Outline each blood parasite and name the species.
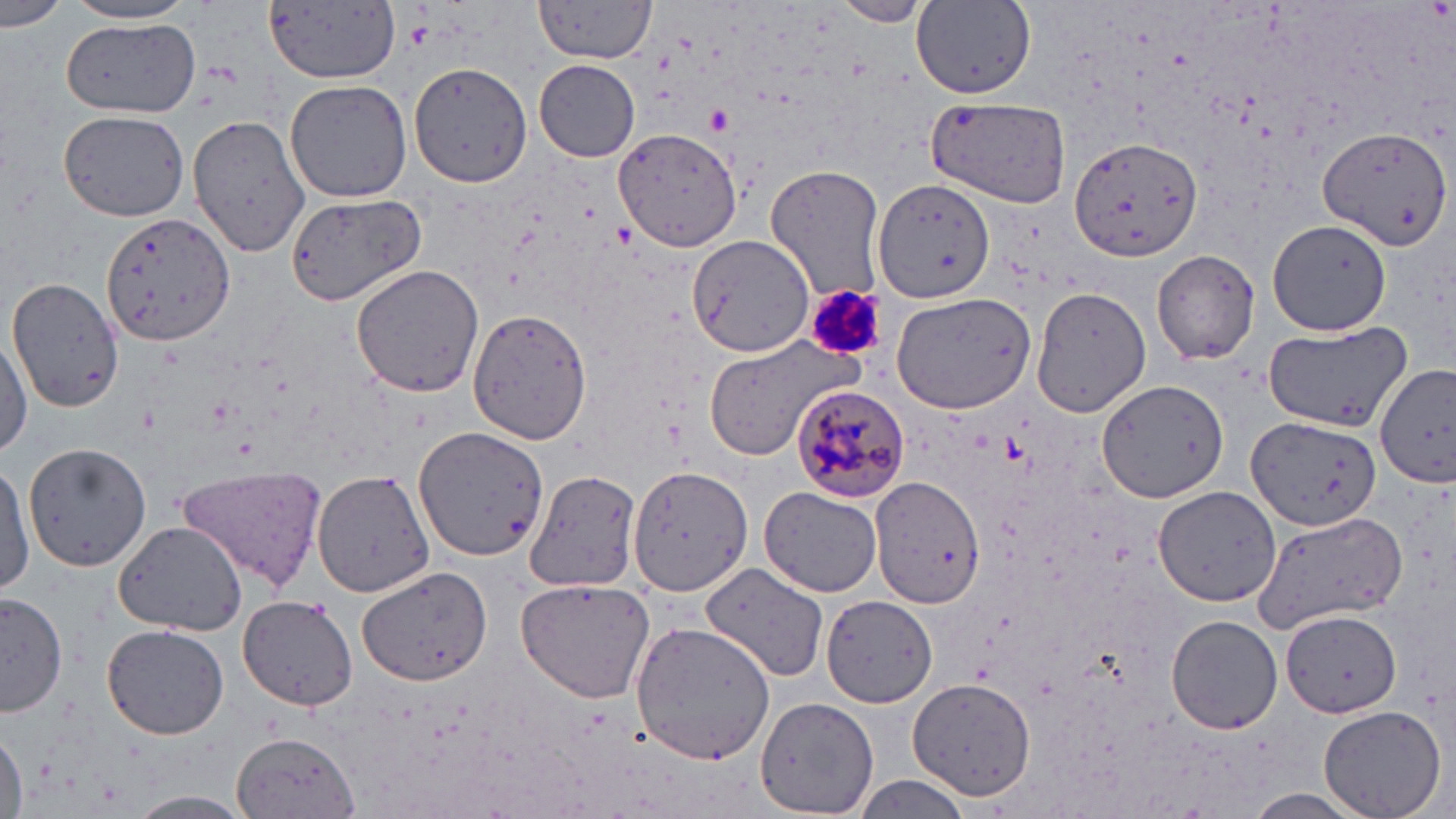

Approximate bounding boxes as (x1,y1)-(x2,y2) corner pairs in pixels.
Plasmodium malariae-infected red blood cells: (793,384)-(912,501).
No Plasmodium falciparum, Plasmodium ovale, Plasmodium vivax, Babesia divergens, or Trypanosoma brucei observed.

{
  "slide_level_diagnosis": "Plasmodium malariae",
  "image_size": "1456×819 pixels",
  "modality": "light microscopy",
  "platelet_locations": "approximate bounding boxes as (x1,y1)-(x2,y2) corner pairs in pixels: (707,108)-(731,133), (802,281)-(884,363)",
  "field_of_view": "one of a larger specimen",
  "magnification": "1000x",
  "stain": "May-Grünwald-Giemsa",
  "uninfected_red_blood_cell_locations": "approximate bounding boxes as (x1,y1)-(x2,y2) corner pairs in pixels: (0,0)-(68,33), (262,0)-(404,85), (830,0)-(933,26), (61,2)-(201,27), (535,2)-(655,63), (913,3)-(1034,98), (63,20)-(200,116), (534,59)-(641,162), (409,61)-(532,189), (285,79)-(413,203), (925,96)-(1072,206), (57,109)-(189,222), (186,112)-(311,260), (1318,125)-(1450,249), (614,128)-(741,251), (1069,135)-(1203,264), (766,167)-(885,302), (875,178)-(996,306), (284,191)-(426,306), (102,210)-(233,348), (1268,219)-(1393,335), (688,234)-(814,355), (1152,248)-(1261,365), (350,264)-(484,398), (7,276)-(124,412), (1032,286)-(1151,417), (892,289)-(1036,411), (468,310)-(593,444), (1261,324)-(1414,433), (0,332)-(32,455), (700,337)-(867,459), (1377,362)-(1455,490), (1094,376)-(1228,503), (1247,417)-(1383,533), (413,424)-(549,560), (25,441)-(152,571), (0,460)-(33,598), (627,463)-(753,595), (176,464)-(327,590), (312,467)-(436,597), (524,467)-(642,591), (870,475)-(985,611), (759,486)-(882,597), (1153,486)-(1281,607), (1251,509)-(1408,631), (114,521)-(246,636), (695,561)-(829,685), (355,565)-(493,687), (516,575)-(658,704), (1,590)-(69,714), (237,594)-(358,711), (819,594)-(940,708), (1282,610)-(1398,715), (1167,616)-(1282,733), (629,620)-(776,765), (102,624)-(229,740), (910,677)-(1037,801), (754,696)-(879,819), (1317,704)-(1447,819), (1,727)-(25,819), (232,732)-(361,819), (854,776)-(980,816), (1241,789)-(1374,817), (125,790)-(259,819)",
  "preparation": "thin blood film"
}